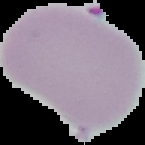

image type = segmented cell region on a black background
result = negative for malaria parasites
image size = 145×145 pixels
preparation = thin blood smear